Give the position of every malaria parasite.
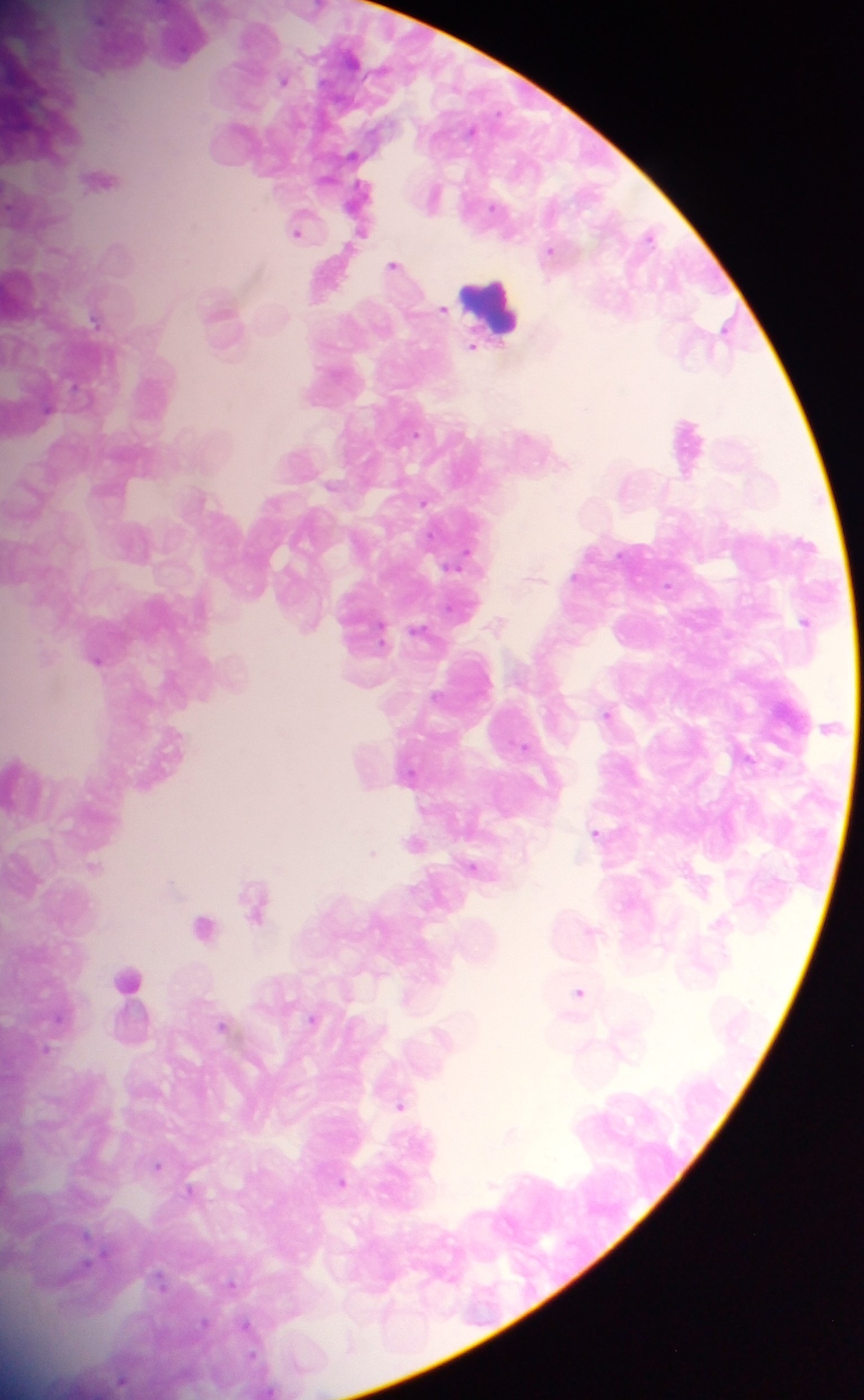
Approximate centers as {x, y} in pixels.
Malaria parasites: {283, 80}, {351, 155}, {297, 230}, {359, 233}, {648, 235}, {549, 250}, {393, 264}, {441, 310}, {94, 319}, {724, 327}, {471, 347}, {422, 501}, {457, 562}, {804, 622}, {419, 632}, {97, 661}, {606, 714}, {525, 747}, {595, 831}, {413, 843}, {371, 852}, {92, 866}, {474, 867}, {170, 884}, {252, 901}, {203, 926}, {578, 992}, {311, 1020}, {222, 1025}, {46, 1049}, {399, 1104}, {509, 1133}, {157, 1166}, {340, 1182}, {189, 1190}, {87, 1237}, {231, 1284}, {247, 1327}, {250, 1354}, {121, 1380}.

Leukocyte locations: {495, 310}, {127, 979}. One field of view. Mobile-phone photograph taken through the microscope. Image is 864×1400 pixels. Sample from Ghana. Thick blood smear.